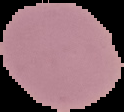

Summary:
  - Image size: 124×112 pixels
  - Malaria status: uninfected
  - Image type: segmented cell region on a black background
  - Preparation: thin blood film